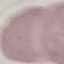

malaria status = uninfected
capture = smartphone through the microscope eyepiece
preparation = thin blood smear
image type = cell patch, automatically extracted from a larger field of view and resized to 64 × 64 pixels
stain = Giemsa